Identify the parasite.
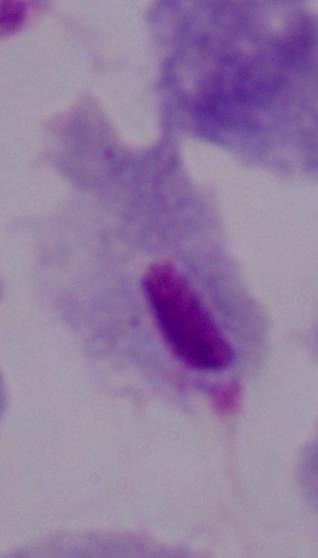
A trichomonad.

Summary:
  - Modality: micrograph
  - Magnification: 1000x